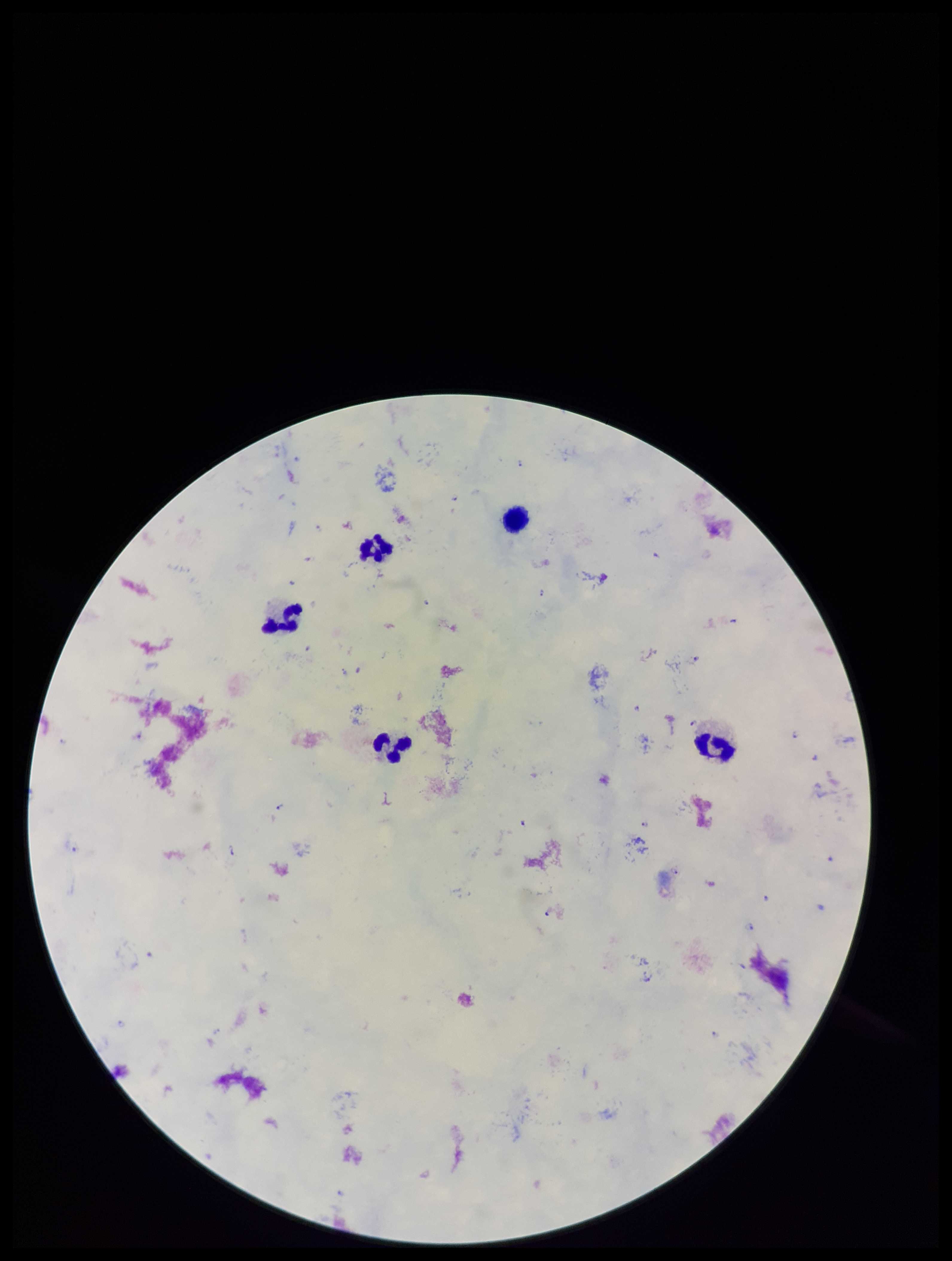
Parasite count: 21. Single field of view. Stained with Giemsa. Patient malaria status: positive. Species reported for this patient: Plasmodium falciparum. Plasmodium parasites: seen. Photographed through the microscope eyepiece with a smartphone camera. Preparation: thick blood smear. Leukocyte count: 5. Image is 952×1261 pixels.